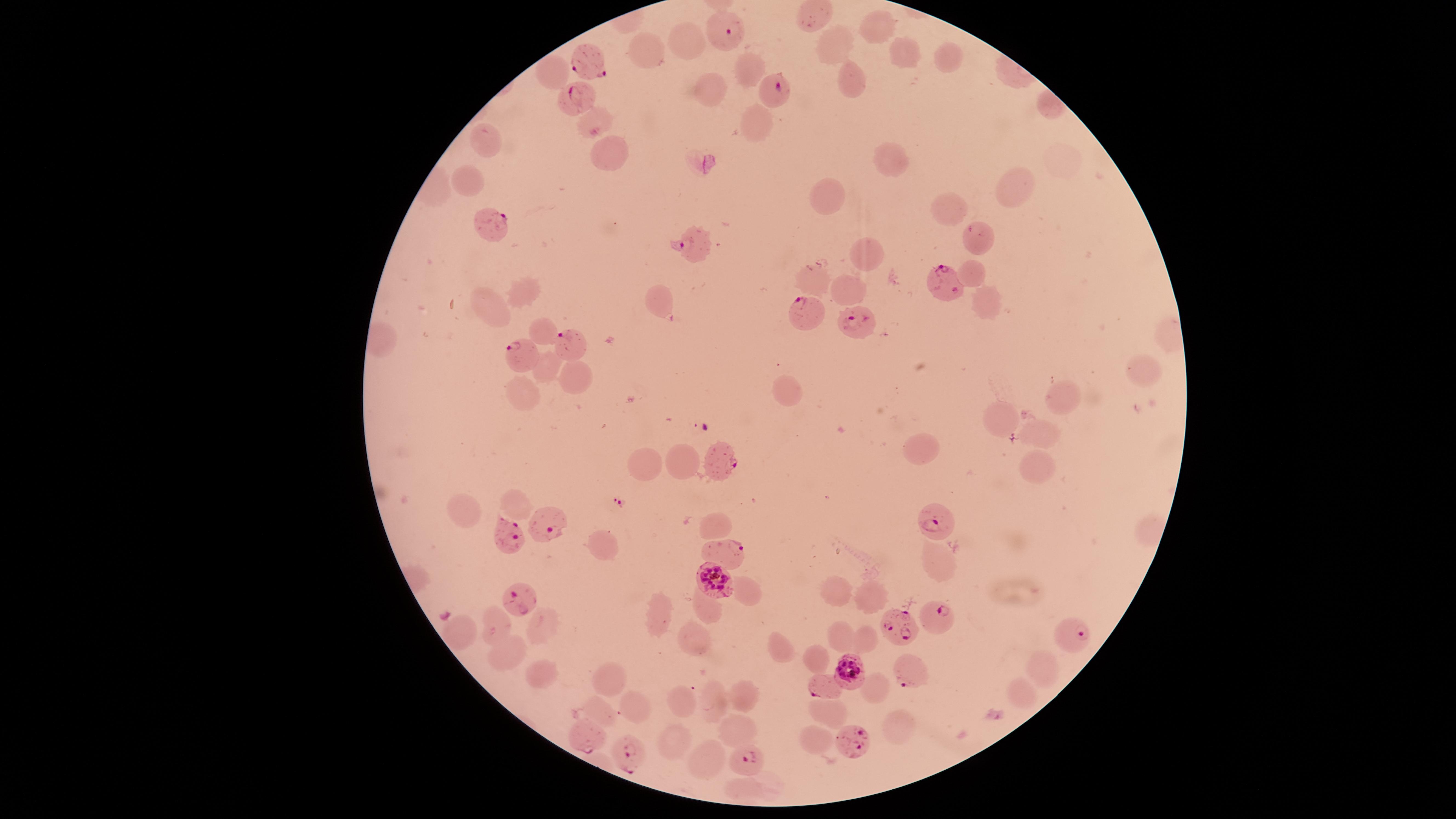

stain = Giemsa
capture = smartphone photograph through the microscope eyepiece
parasitized red blood cells = approximate marker points as [x, y] in pixels: [724, 30], [585, 56], [773, 89], [574, 101], [489, 221], [695, 244], [945, 283], [807, 312], [856, 321], [569, 344], [521, 355], [721, 456], [546, 519], [935, 523], [506, 534], [729, 551], [712, 576], [519, 600], [932, 616], [903, 628], [1075, 636], [849, 669], [909, 674], [820, 686], [588, 739], [848, 741], [624, 749], [752, 759]
species = Plasmodium falciparum
field of view = single
image size = 1456×819 pixels
presence = malaria parasites seen
uninfected red blood cells = approximate marker points as [x, y] in pixels: [816, 8], [880, 23], [683, 39], [832, 45], [645, 54], [904, 55], [950, 59], [749, 67], [547, 75], [851, 78], [708, 92], [590, 119], [748, 120], [488, 141], [609, 148], [888, 161], [468, 180], [1015, 192], [831, 199], [951, 210], [978, 244], [868, 252], [974, 270], [813, 280], [846, 290], [524, 294], [662, 297], [990, 298], [489, 310], [543, 332], [542, 367], [1140, 367], [577, 375], [524, 389], [786, 392], [1068, 394], [1002, 418], [1033, 435], [918, 451], [680, 458], [644, 463], [1033, 468], [517, 502], [462, 508], [713, 526], [606, 542], [935, 561], [742, 590], [838, 591], [871, 598], [707, 607], [661, 613], [493, 625], [537, 628], [459, 630], [838, 635], [689, 637], [865, 638], [782, 645], [506, 653], [814, 654], [1040, 669], [528, 670], [613, 680], [869, 686], [1017, 693], [736, 695], [681, 697], [635, 704], [714, 705], [604, 706], [830, 708], [898, 724], [740, 729], [814, 737], [678, 740], [706, 761], [747, 791]
visible region = circular
preparation = thin blood film